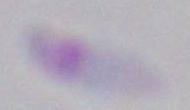 Micrograph. Captured at 1000x magnification. Toxoplasma gondii is seen.